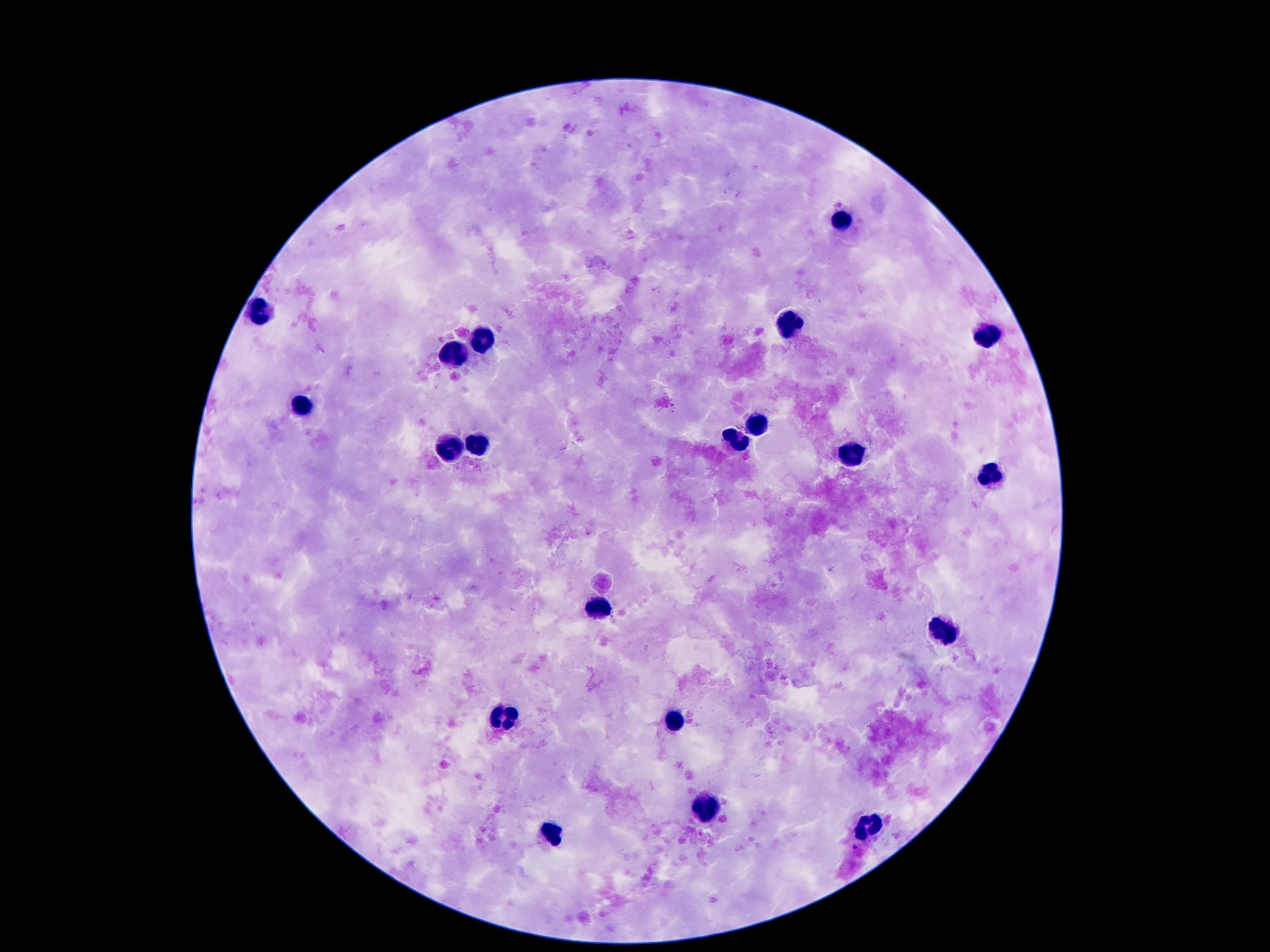 Approximate centers as (x, y) in pixels. Leukocyte locations: (845, 223), (261, 314), (792, 326), (988, 334), (481, 342), (456, 355), (302, 410), (759, 424), (739, 441), (479, 443), (448, 447), (853, 455), (995, 479), (599, 606), (945, 632), (505, 719), (675, 721), (708, 809), (870, 828), (552, 833). Giemsa stain. Image is 1270×952 pixels. One field from this slide. Thick blood smear. 100x magnification. Patient malaria status: not infected. Photographed through the microscope eyepiece with a smartphone camera.